Classify this cell by malaria status.
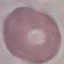
It is uninfected.

Giemsa stain. Thin blood smear. Acquired by smartphone through the microscope eyepiece. Cell patch, automatically extracted from a larger field of view and resized to 64 × 64 pixels.